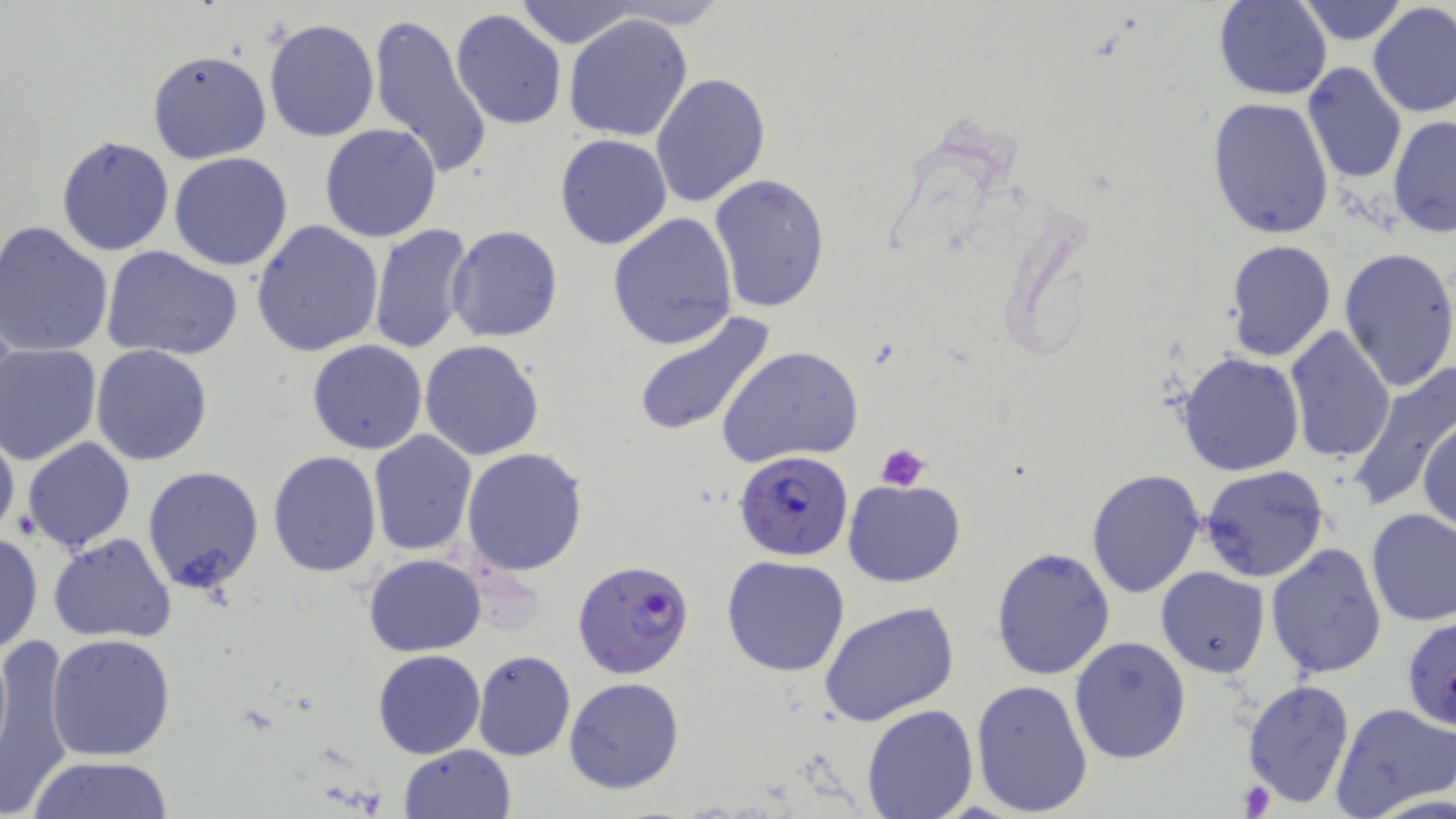
{
  "slide_level_diagnosis": "Plasmodium falciparum",
  "field_of_view": "single",
  "platelet_locations": "approximate bounding boxes as named x1/y1/x2/y2 corners in pixels: (x1=875, y1=444, x2=932, y2=491), (x1=1240, y1=780, x2=1275, y2=815)",
  "stain": "May-Grünwald-Giemsa",
  "preparation": "thin blood film",
  "plasmodium_falciparum_infected_red_blood_cell_locations": "approximate bounding boxes as named x1/y1/x2/y2 corners in pixels: (x1=733, y1=450, x2=853, y2=560), (x1=573, y1=560, x2=696, y2=680)",
  "image_size": "1456×819 pixels",
  "modality": "light microscopy",
  "uninfected_red_blood_cell_locations": "approximate bounding boxes as named x1/y1/x2/y2 corners in pixels: (x1=513, y1=0, x2=642, y2=49), (x1=596, y1=0, x2=730, y2=28), (x1=1213, y1=1, x2=1332, y2=99), (x1=1295, y1=1, x2=1409, y2=47), (x1=1367, y1=3, x2=1456, y2=118), (x1=450, y1=8, x2=566, y2=129), (x1=369, y1=12, x2=495, y2=181), (x1=563, y1=12, x2=695, y2=142), (x1=262, y1=18, x2=378, y2=142), (x1=147, y1=48, x2=272, y2=165), (x1=1301, y1=63, x2=1408, y2=186), (x1=650, y1=73, x2=773, y2=211), (x1=1205, y1=96, x2=1334, y2=240), (x1=1388, y1=117, x2=1455, y2=238), (x1=319, y1=123, x2=443, y2=243), (x1=56, y1=134, x2=175, y2=257), (x1=554, y1=134, x2=673, y2=251), (x1=168, y1=152, x2=294, y2=271), (x1=709, y1=172, x2=833, y2=315), (x1=607, y1=212, x2=739, y2=351), (x1=1, y1=220, x2=116, y2=359), (x1=251, y1=220, x2=384, y2=357), (x1=368, y1=223, x2=475, y2=357), (x1=445, y1=225, x2=564, y2=344), (x1=1225, y1=239, x2=1336, y2=362), (x1=99, y1=245, x2=244, y2=363), (x1=1339, y1=246, x2=1456, y2=395), (x1=630, y1=307, x2=778, y2=438), (x1=1284, y1=326, x2=1395, y2=465), (x1=307, y1=340, x2=428, y2=455), (x1=419, y1=340, x2=545, y2=460), (x1=91, y1=344, x2=214, y2=466), (x1=718, y1=344, x2=864, y2=466), (x1=1, y1=346, x2=101, y2=465), (x1=1177, y1=352, x2=1305, y2=477), (x1=1347, y1=361, x2=1456, y2=515), (x1=1417, y1=414, x2=1455, y2=534), (x1=0, y1=422, x2=20, y2=545), (x1=367, y1=431, x2=479, y2=556), (x1=22, y1=437, x2=134, y2=553), (x1=460, y1=447, x2=589, y2=576), (x1=266, y1=450, x2=381, y2=578), (x1=141, y1=465, x2=264, y2=595), (x1=1200, y1=465, x2=1329, y2=582), (x1=1086, y1=468, x2=1208, y2=597), (x1=844, y1=479, x2=966, y2=586), (x1=1365, y1=507, x2=1456, y2=628), (x1=0, y1=531, x2=44, y2=656), (x1=47, y1=532, x2=178, y2=644), (x1=1266, y1=544, x2=1387, y2=679), (x1=990, y1=545, x2=1117, y2=683), (x1=362, y1=554, x2=486, y2=655), (x1=722, y1=554, x2=852, y2=676), (x1=1157, y1=566, x2=1269, y2=677), (x1=1110, y1=589, x2=1231, y2=733), (x1=818, y1=601, x2=959, y2=727), (x1=1401, y1=616, x2=1456, y2=735), (x1=0, y1=631, x2=77, y2=819), (x1=46, y1=632, x2=177, y2=760), (x1=1070, y1=636, x2=1191, y2=764), (x1=374, y1=650, x2=486, y2=759), (x1=472, y1=650, x2=577, y2=761), (x1=564, y1=676, x2=686, y2=795), (x1=971, y1=678, x2=1094, y2=817), (x1=1242, y1=678, x2=1356, y2=806), (x1=1331, y1=702, x2=1456, y2=819), (x1=862, y1=703, x2=978, y2=818), (x1=398, y1=744, x2=516, y2=819), (x1=24, y1=756, x2=179, y2=817)",
  "magnification": "1000x"
}